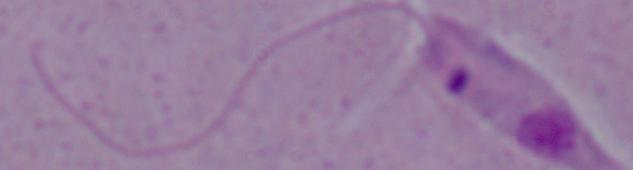
identification: Leishmania
magnification: 1000x
modality: micrograph